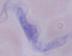
1000x magnification. Micrograph. A trypanosome is seen.